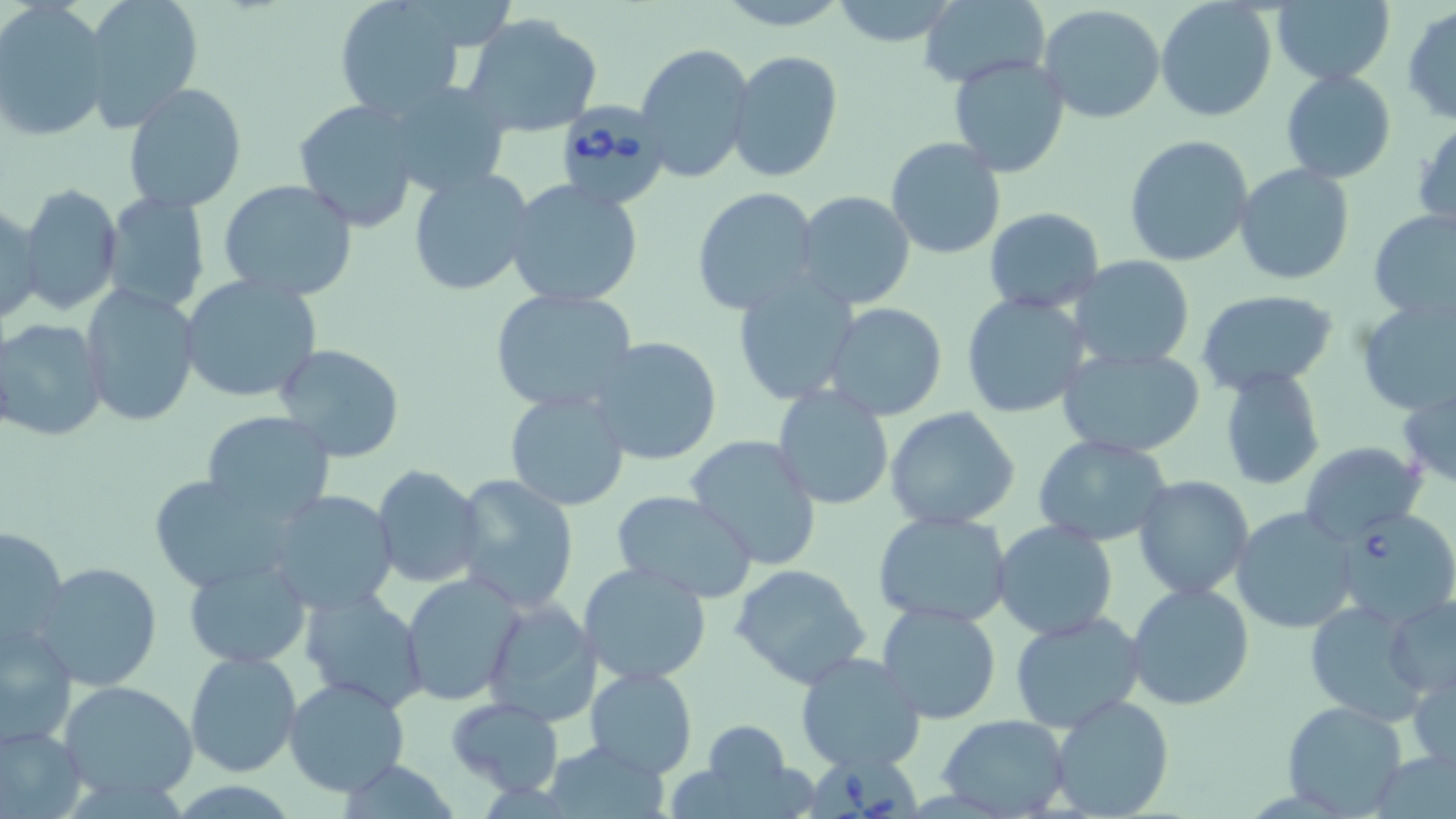

slide-level diagnosis = Babesia divergens
stain = May-Grünwald-Giemsa
field of view = single
modality = optical microscopy
image size = 1456×819 pixels
uninfected red blood cell locations = approximate bounding boxes as (x1, y1, x2, y2) in pixels: (77, 0, 205, 134), (333, 0, 470, 119), (716, 0, 852, 30), (828, 0, 960, 48), (1156, 0, 1278, 123), (916, 1, 1049, 84), (1270, 1, 1394, 86), (1038, 5, 1167, 126), (1402, 6, 1456, 124), (0, 7, 112, 143), (462, 13, 604, 139), (635, 44, 757, 184), (727, 50, 843, 183), (947, 54, 1071, 177), (1281, 70, 1397, 184), (379, 77, 515, 200), (122, 82, 249, 212), (293, 99, 420, 231), (1413, 118, 1456, 230), (1124, 136, 1252, 266), (884, 138, 1006, 260), (1233, 164, 1355, 285), (407, 167, 538, 299), (218, 179, 358, 301), (504, 179, 643, 310), (17, 182, 124, 316), (691, 185, 821, 316), (102, 188, 212, 314), (794, 192, 918, 310), (1, 204, 43, 326), (984, 208, 1104, 312), (1368, 210, 1456, 320), (1070, 256, 1196, 371), (177, 273, 324, 406), (732, 274, 861, 405), (79, 284, 200, 427), (490, 287, 637, 413), (1196, 290, 1338, 392), (960, 291, 1092, 421), (1355, 296, 1456, 416), (823, 303, 948, 420), (0, 317, 108, 442), (587, 337, 725, 467), (1058, 343, 1207, 457), (273, 345, 407, 462), (1217, 363, 1328, 490), (1399, 379, 1456, 490), (771, 383, 896, 513), (504, 389, 630, 511), (883, 406, 1023, 532), (201, 412, 336, 524), (1032, 434, 1173, 547), (686, 436, 823, 572), (1300, 442, 1425, 545), (371, 465, 484, 587), (146, 474, 302, 592), (450, 474, 580, 613), (1133, 475, 1255, 602), (265, 490, 400, 614), (610, 490, 759, 603), (1231, 507, 1357, 634), (873, 511, 1013, 628), (991, 520, 1118, 642), (1, 523, 69, 650), (182, 555, 313, 668), (34, 560, 164, 692), (577, 562, 711, 686), (728, 562, 874, 690), (400, 574, 524, 705), (1126, 583, 1255, 712), (300, 587, 429, 713), (1384, 594, 1456, 700), (481, 596, 600, 727), (1302, 599, 1428, 722), (876, 602, 1002, 723), (1009, 611, 1146, 733), (1, 622, 78, 742), (184, 651, 303, 778), (794, 651, 927, 775), (1409, 662, 1455, 773), (583, 665, 697, 777), (284, 676, 410, 798), (59, 679, 198, 804), (1050, 694, 1175, 818), (445, 697, 565, 797), (1282, 700, 1407, 816), (937, 714, 1071, 817), (697, 721, 797, 810), (0, 722, 86, 817), (542, 739, 671, 816)
Babesia divergens-infected red blood cell locations = approximate bounding boxes as (x1, y1, x2, y2) in pixels: (550, 97, 673, 212), (1333, 507, 1456, 625), (810, 746, 924, 819)
magnification = 1000x
preparation = thin blood smear